Outline each blood parasite and name the species.
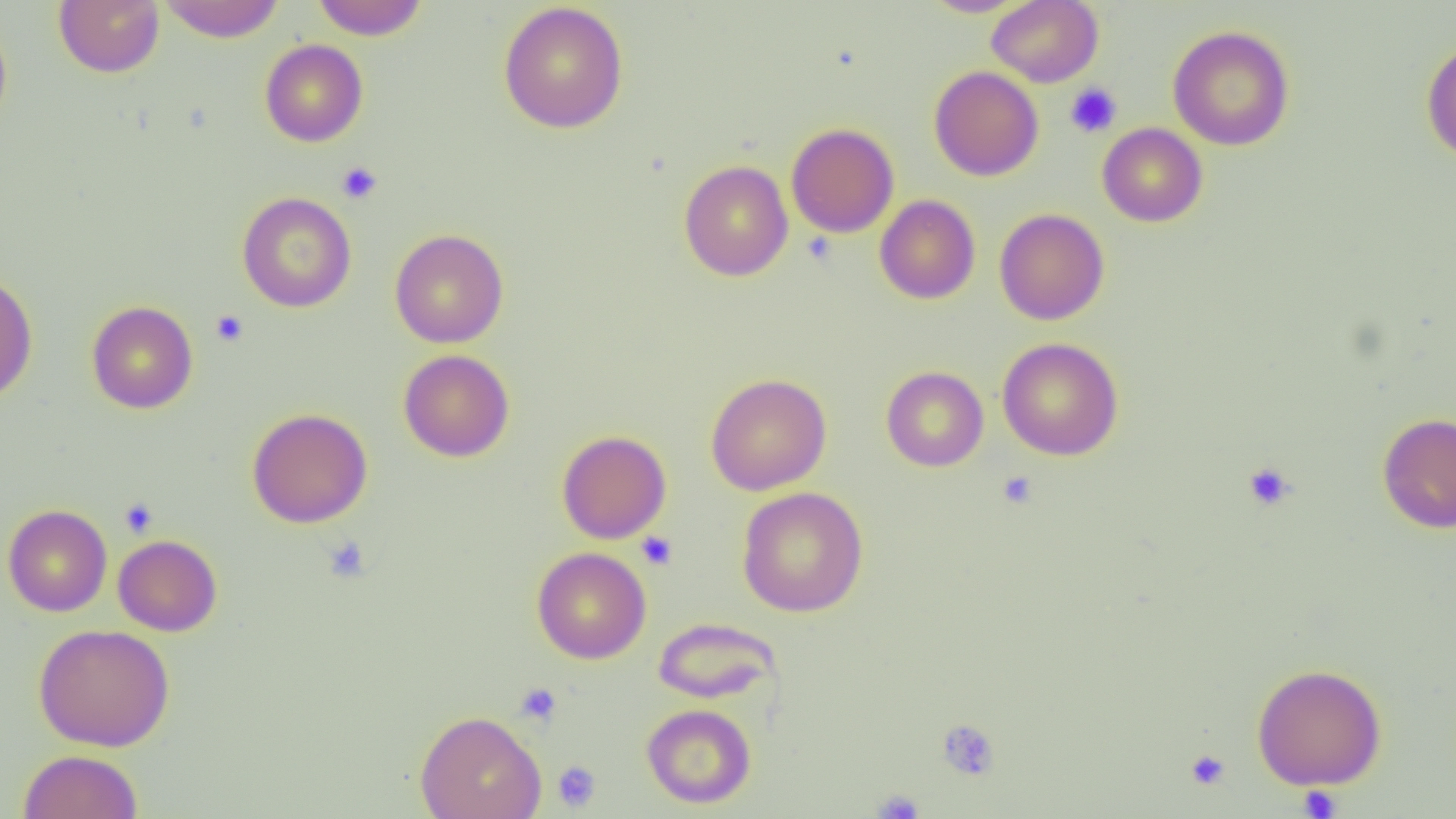

No blood parasites seen.

{
  "slide_level_diagnosis": "negative for blood parasites",
  "image_size": "1456×819 pixels",
  "modality": "optical microscopy",
  "platelet_locations": "approximate bounding boxes as named x1/y1/x2/y2 corners in pixels: (x1=1064, y1=82, x2=1122, y2=138), (x1=336, y1=161, x2=383, y2=204), (x1=210, y1=309, x2=249, y2=347), (x1=1243, y1=462, x2=1296, y2=510), (x1=998, y1=470, x2=1038, y2=509), (x1=119, y1=497, x2=158, y2=538), (x1=636, y1=531, x2=677, y2=570), (x1=322, y1=536, x2=370, y2=583), (x1=515, y1=682, x2=562, y2=726), (x1=936, y1=718, x2=1000, y2=781), (x1=1185, y1=749, x2=1231, y2=790), (x1=552, y1=760, x2=601, y2=811), (x1=1297, y1=785, x2=1343, y2=818), (x1=872, y1=788, x2=925, y2=818)",
  "uninfected_red_blood_cell_locations": "approximate bounding boxes as named x1/y1/x2/y2 corners in pixels: (x1=54, y1=0, x2=164, y2=77), (x1=156, y1=0, x2=286, y2=42), (x1=311, y1=0, x2=429, y2=39), (x1=920, y1=0, x2=1029, y2=17), (x1=987, y1=0, x2=1103, y2=87), (x1=498, y1=2, x2=629, y2=133), (x1=0, y1=18, x2=13, y2=134), (x1=1168, y1=25, x2=1295, y2=151), (x1=260, y1=39, x2=368, y2=147), (x1=1421, y1=40, x2=1456, y2=163), (x1=928, y1=66, x2=1044, y2=181), (x1=785, y1=123, x2=899, y2=238), (x1=1097, y1=123, x2=1208, y2=227), (x1=679, y1=160, x2=793, y2=281), (x1=236, y1=191, x2=356, y2=312), (x1=874, y1=195, x2=980, y2=304), (x1=994, y1=208, x2=1109, y2=325), (x1=389, y1=228, x2=508, y2=348), (x1=0, y1=269, x2=38, y2=403), (x1=86, y1=301, x2=198, y2=414), (x1=997, y1=337, x2=1123, y2=460), (x1=398, y1=349, x2=514, y2=462), (x1=881, y1=366, x2=989, y2=471), (x1=705, y1=373, x2=832, y2=495), (x1=247, y1=407, x2=373, y2=528), (x1=1377, y1=412, x2=1456, y2=534), (x1=557, y1=430, x2=671, y2=544), (x1=737, y1=486, x2=869, y2=617), (x1=2, y1=504, x2=112, y2=617), (x1=113, y1=534, x2=222, y2=636), (x1=531, y1=547, x2=651, y2=664), (x1=654, y1=617, x2=781, y2=704), (x1=32, y1=623, x2=175, y2=751), (x1=1251, y1=663, x2=1387, y2=790), (x1=641, y1=703, x2=756, y2=808), (x1=414, y1=710, x2=546, y2=819), (x1=17, y1=749, x2=143, y2=819)",
  "preparation": "thin blood film",
  "magnification": "1000x",
  "field_of_view": "single"
}